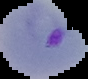
Image is 88×79 pixels. Malaria status: parasitized. From a thin blood film. Cell region segmented out of the field of view; the surrounding area is masked to black.